Locate and identify every blood parasite.
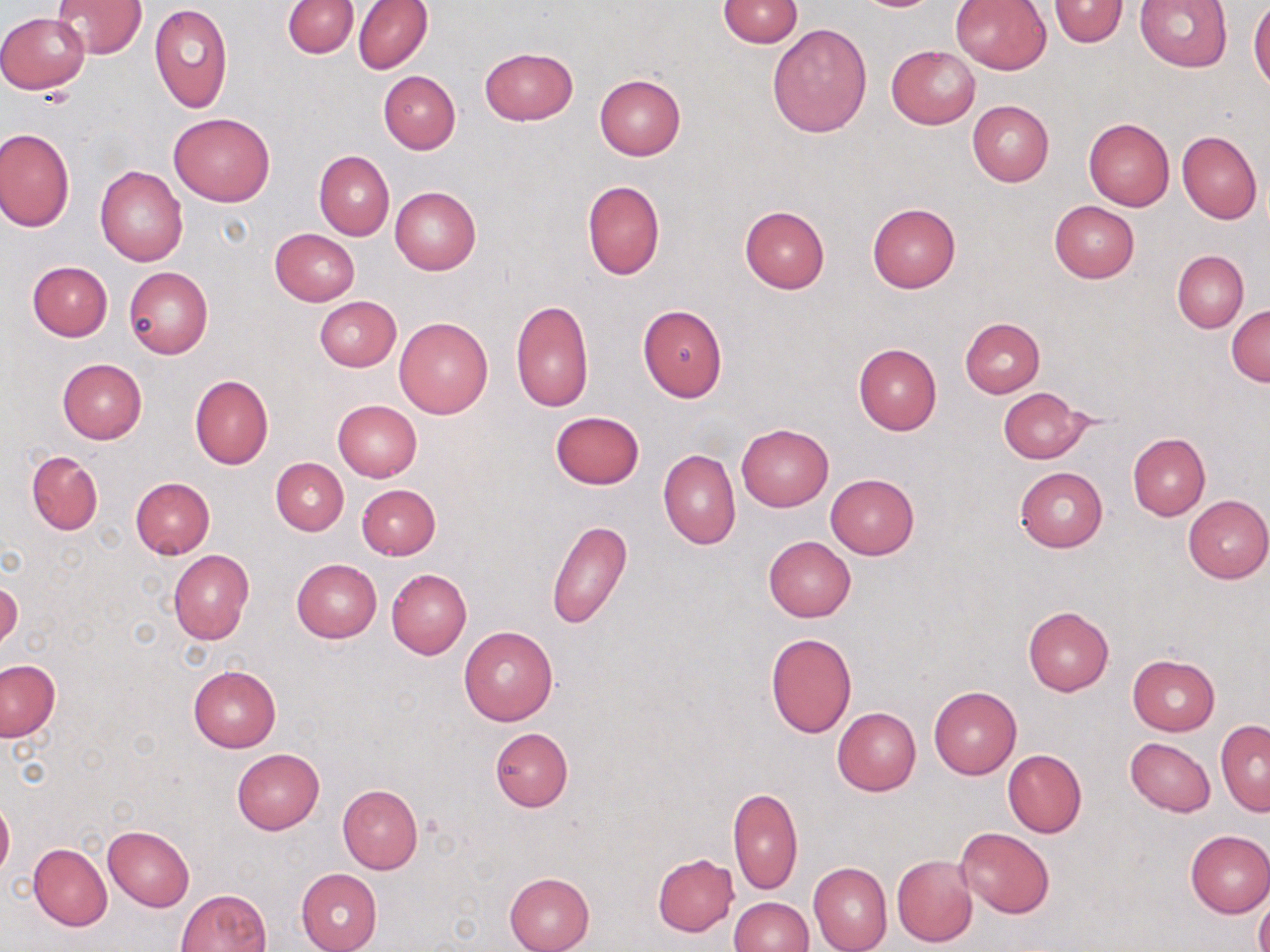

No blood parasites observed.

Summary:
  - Coordinate format: approximate bounding boxes as (x1, y1, x2, y2) in pixels
  - Uninfected red blood cell locations: (283, 0, 359, 58), (353, 0, 432, 74), (719, 0, 803, 47), (1048, 0, 1128, 48), (51, 1, 146, 59), (950, 1, 1051, 74), (1133, 1, 1234, 70), (1249, 1, 1270, 90), (149, 3, 232, 114), (0, 11, 90, 92), (767, 22, 872, 136), (886, 45, 980, 129), (479, 47, 578, 125), (378, 71, 461, 154), (593, 74, 686, 160), (967, 100, 1054, 187), (170, 114, 275, 205), (1084, 117, 1175, 211), (0, 127, 74, 232), (1177, 130, 1263, 223), (314, 150, 394, 240), (95, 167, 188, 266), (581, 179, 666, 280), (389, 185, 481, 276), (1049, 200, 1141, 282), (867, 203, 962, 293), (739, 205, 830, 293), (271, 228, 358, 305), (1173, 250, 1248, 332), (27, 261, 113, 341), (124, 266, 213, 359), (314, 296, 401, 372), (511, 301, 593, 411), (638, 304, 728, 401), (1228, 305, 1270, 386), (394, 317, 492, 418), (960, 318, 1045, 398), (853, 343, 942, 435), (57, 358, 147, 444), (189, 374, 274, 469), (998, 387, 1091, 464), (332, 400, 423, 481), (550, 410, 645, 489), (736, 423, 834, 511), (1128, 433, 1210, 520), (658, 449, 740, 549), (27, 450, 102, 535), (271, 458, 349, 535), (1015, 466, 1107, 551), (826, 474, 919, 559), (130, 478, 214, 559), (357, 484, 441, 560), (1183, 495, 1270, 583), (547, 519, 631, 629), (763, 536, 856, 621), (168, 550, 253, 645), (291, 559, 382, 643), (386, 568, 472, 660), (1, 578, 21, 649), (1022, 605, 1113, 695), (459, 626, 558, 725), (765, 633, 857, 738), (1127, 654, 1220, 735), (0, 661, 61, 741), (188, 665, 281, 753), (929, 686, 1021, 780), (832, 707, 921, 795), (1215, 720, 1270, 815), (490, 727, 573, 812), (1125, 737, 1216, 816), (231, 748, 324, 834), (1003, 749, 1086, 838), (336, 784, 424, 874), (727, 788, 802, 895), (0, 798, 13, 881), (103, 825, 195, 911), (955, 827, 1054, 919), (1184, 830, 1269, 917), (30, 837, 190, 919), (28, 843, 112, 931), (652, 853, 739, 936), (892, 854, 978, 947), (808, 862, 892, 952), (295, 868, 381, 951), (504, 872, 595, 952), (176, 888, 271, 952), (1256, 890, 1270, 952), (728, 897, 812, 952)
  - Slide-level diagnosis: negative for blood parasites
  - Stain: May-Grünwald-Giemsa
  - Modality: light microscopy
  - Magnification: 1000x
  - Preparation: thin blood smear
  - Image size: 1270×952 pixels
  - Field of view: single